Report the malaria status of this cell.
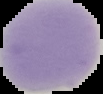

It is uninfected.

image_type: cell region segmented out of the field of view; surrounding area masked to black
preparation: thin blood film
image_size: 103×94 pixels